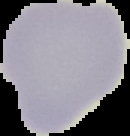 Malaria status: uninfected. The area outside the segmented cell region is set to black. From a thin blood smear. Image is 130×136 pixels.